Evaluate for malaria.
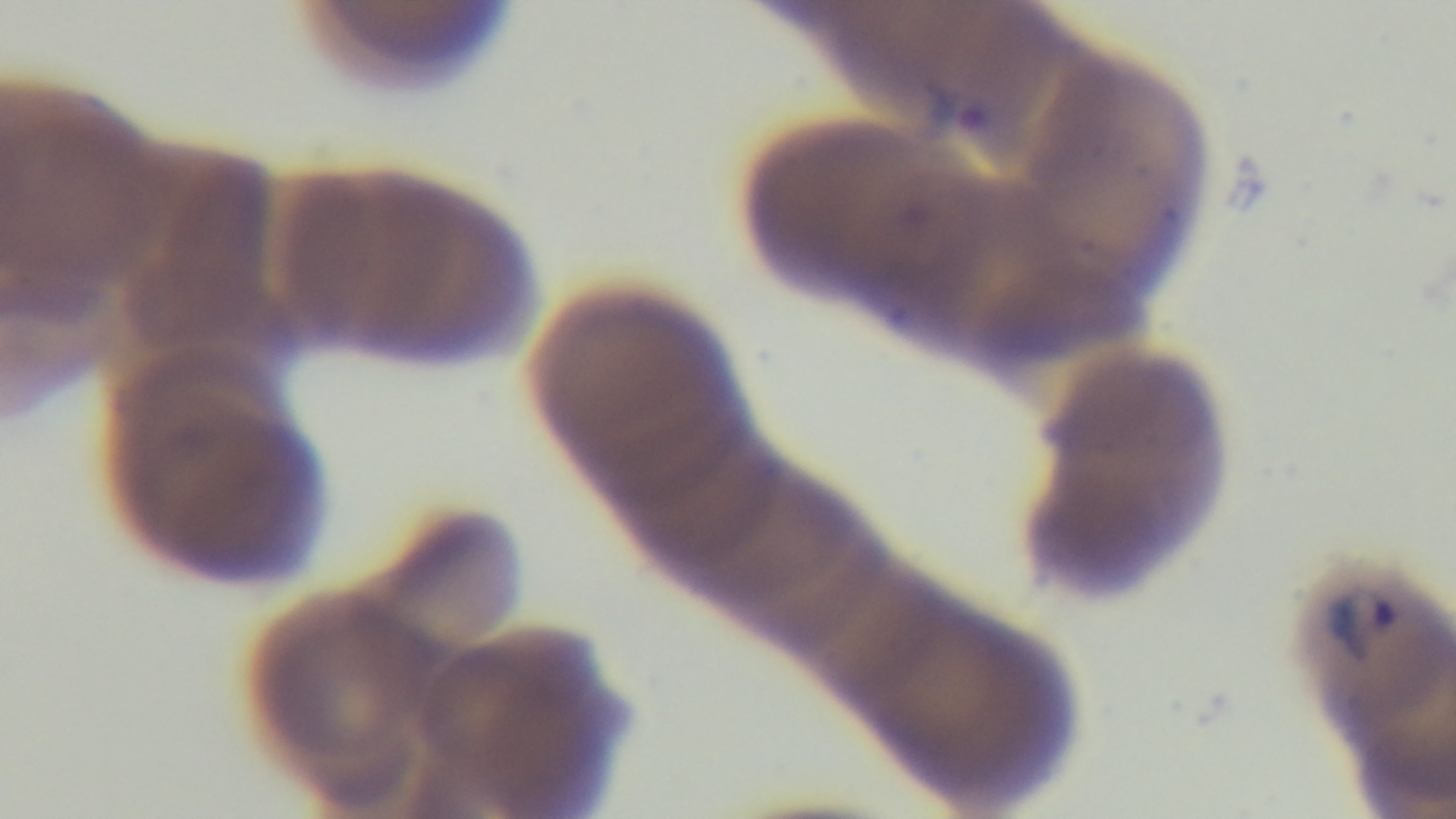

It is infected.

100x oil-immersion objective. Giemsa-stained. Preparation: thin. One field from the slide. Photomicrograph. Mounted 4K digital camera.